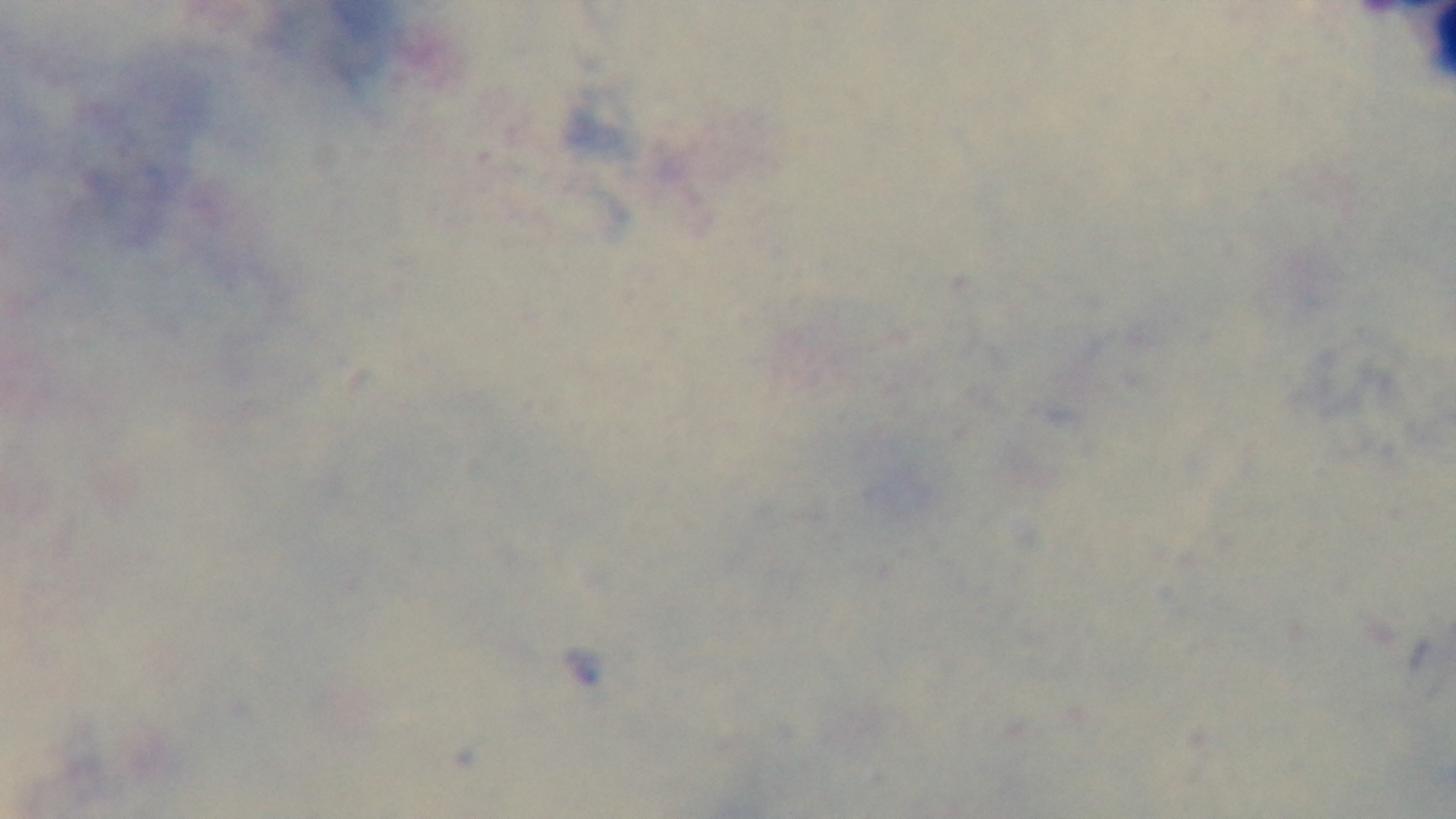
Mounted 4K digital camera. Malaria status: negative. One field from the slide. Photomicrograph. Giemsa-stained. Oil-immersion objective, 100x. Preparation: thick smear.